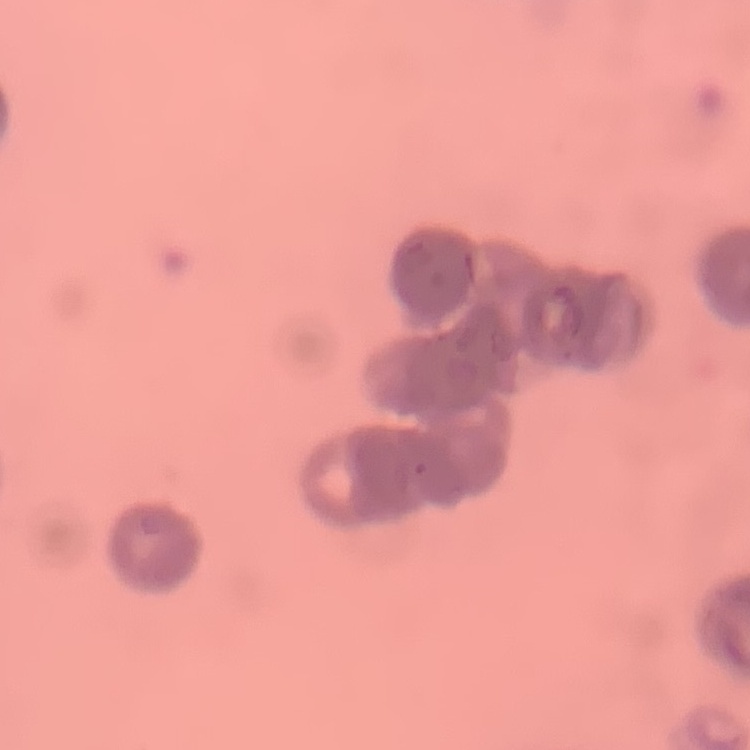
Summary:
  - Red blood cell morphology: rouleaux formation
  - Stain: Field's or Giemsa
  - Preparation: thin blood film
  - Image type: one tile cut from a larger photomicrograph